Draw a bounding box around every parasitised red blood cell, every trophozoite, every gametocyte, every leukocyte, and every artifact (platelet-like body, stain precipitate, or debris).
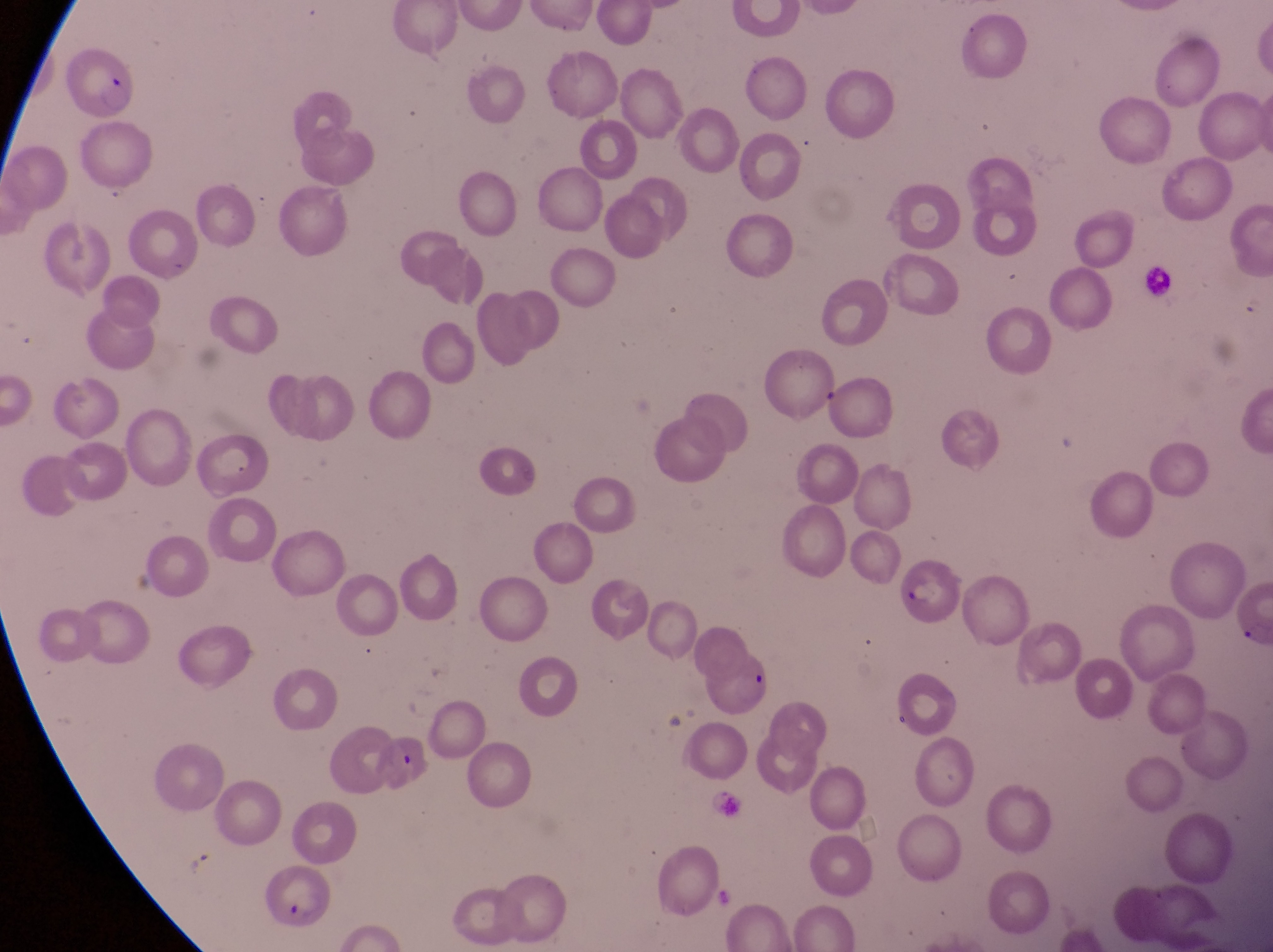

Approximate bounding boxes as [left, top, right, bottom] in pixels.
Parasitised red blood cells: [702, 651, 777, 725], [257, 867, 337, 930].
No leukocytes observed.

One field of view. At a magnification of 1000x. Thin blood smear. Captured by a smartphone held over the eyepiece of an Olympus CX-23 microscope. Image is 1273×952 pixels. Sample from Uganda.